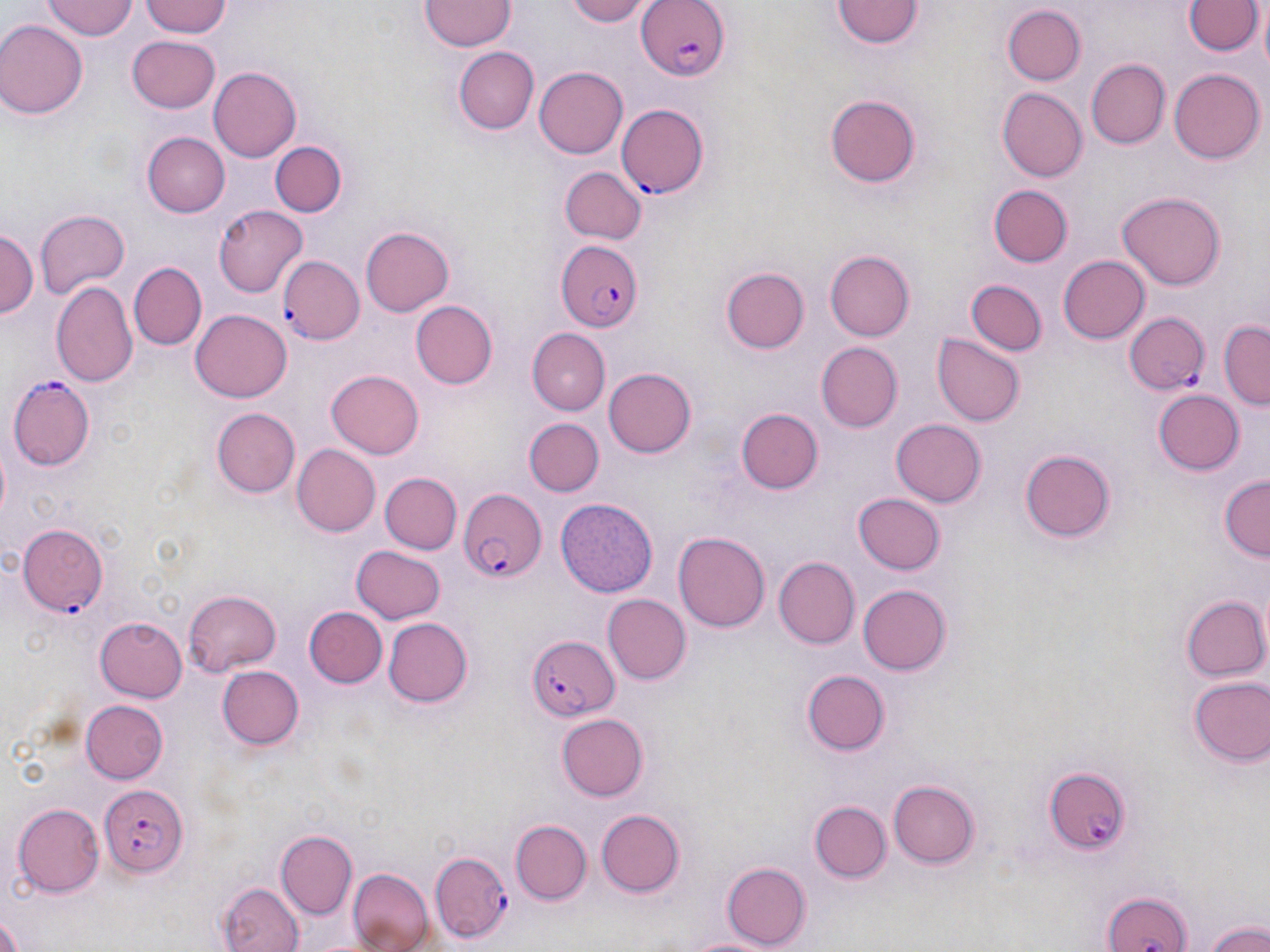

Summary:
  - Coordinate format: approximate bounding boxes as (x1,y1)-(x2,y2) corner pairs in pixels
  - Plasmodium falciparum-infected red blood cell locations: (635,0)-(730,83), (616,103)-(709,200), (554,239)-(641,332), (280,256)-(364,344), (1123,309)-(1211,395), (8,378)-(95,470), (456,487)-(546,583), (17,524)-(108,615), (528,635)-(619,722), (1042,766)-(1130,854), (99,781)-(189,876), (428,851)-(513,940), (1103,888)-(1191,952)
  - Uninfected red blood cell locations: (43,0)-(136,40), (141,0)-(232,37), (422,0)-(515,50), (567,0)-(653,28), (1186,1)-(1259,57), (835,2)-(924,50), (1255,3)-(1269,80), (1001,6)-(1086,88), (1,21)-(87,119), (126,35)-(223,111), (454,48)-(539,134), (1088,59)-(1170,149), (534,65)-(627,157), (209,66)-(301,162), (1168,67)-(1264,164), (225,77)-(328,201), (996,87)-(1087,183), (824,91)-(924,186), (141,132)-(229,218), (271,141)-(348,218), (559,165)-(646,243), (989,187)-(1072,267), (1115,191)-(1226,291), (215,205)-(308,298), (36,209)-(131,298), (359,226)-(454,316), (1,228)-(36,319), (823,250)-(914,341), (1058,254)-(1148,342), (128,262)-(206,350), (721,268)-(809,353), (966,279)-(1047,357), (51,282)-(137,387), (409,300)-(497,390), (191,310)-(292,401), (1220,319)-(1270,408), (526,329)-(608,416), (933,332)-(1024,426), (818,342)-(903,432), (327,368)-(424,457), (604,368)-(698,458), (1154,388)-(1245,474), (215,408)-(301,497), (739,409)-(822,494), (524,417)-(603,495), (891,419)-(986,507), (293,444)-(381,536), (1016,447)-(1118,542), (379,472)-(461,554), (1219,476)-(1269,562), (853,493)-(947,576), (556,496)-(659,597), (673,529)-(771,635), (349,545)-(445,624), (773,558)-(859,649), (856,583)-(950,675), (182,590)-(279,675), (602,594)-(692,685), (1181,595)-(1268,683), (302,607)-(386,690), (96,615)-(190,701), (381,617)-(471,707), (216,664)-(305,750), (803,668)-(890,755), (1186,673)-(1269,767), (80,701)-(167,784), (555,713)-(648,801), (887,778)-(982,868), (808,801)-(891,884), (12,803)-(104,897), (595,809)-(685,897), (510,820)-(591,904), (276,826)-(357,921), (722,861)-(810,949), (346,869)-(433,952), (218,881)-(306,952), (0,912)-(24,952), (1203,918)-(1270,952), (679,933)-(780,952)
  - Slide-level diagnosis: Plasmodium falciparum
  - Magnification: 1000x
  - Preparation: thin blood smear
  - Stain: May-Grünwald-Giemsa
  - Modality: optical microscopy
  - Image size: 1270×952 pixels
  - Field of view: one of a larger specimen